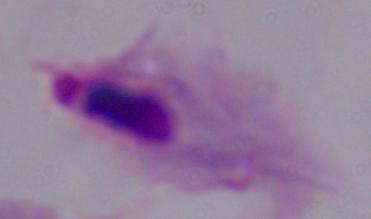
{
  "identification": "trichomonad",
  "magnification": "1000x",
  "modality": "photomicrograph"
}